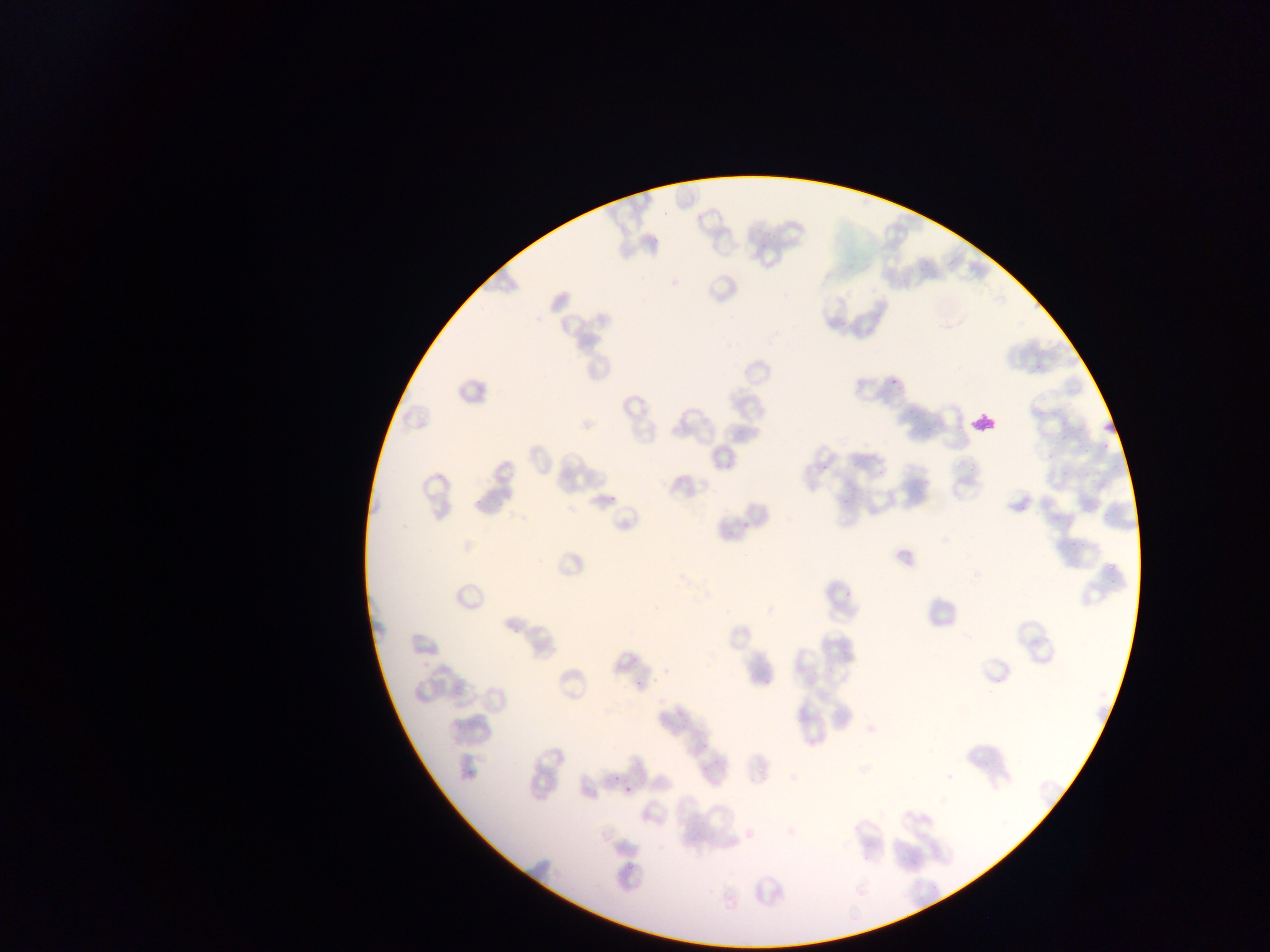 Approximate bounding boxes as left top right bottom in pixels. Leukocyte locations: 967 408 1001 440. Collected in Ghana. Photographed through a microscope with a mobile-phone camera. Thin blood smear. Image is 1270×952 pixels. One field of view.